Identify the preparation type.
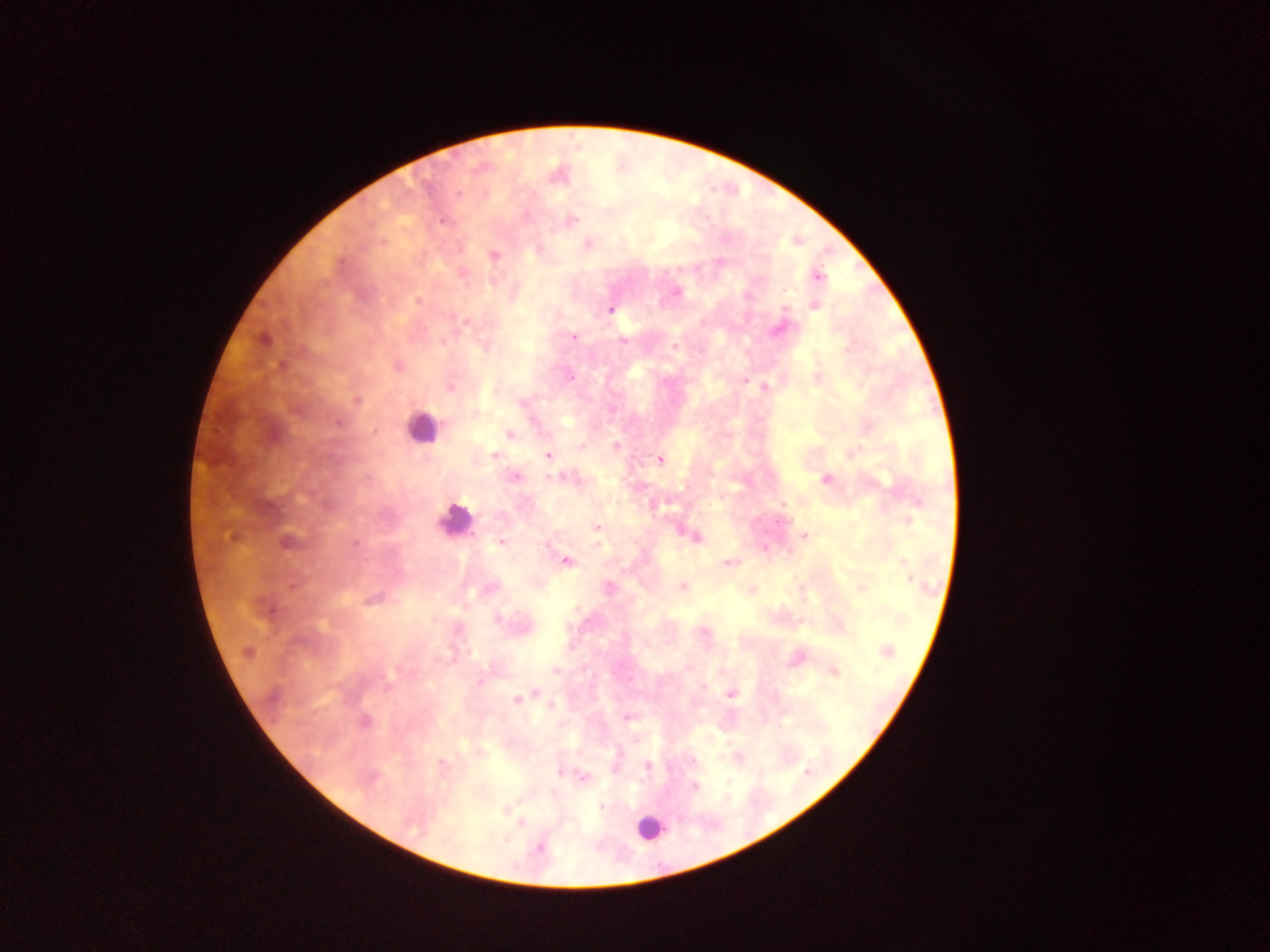

Thick blood film.

Approximate centers as {x, y} in pixels.
Summary:
  - Leukocyte locations: {421, 427}, {456, 526}, {643, 827}
  - Plasmodium parasite locations: {457, 192}, {571, 218}, {588, 244}, {817, 277}, {814, 306}, {609, 309}, {465, 320}, {575, 337}, {620, 339}, {674, 346}, {815, 377}, {744, 380}, {764, 386}, {519, 399}, {510, 433}, {615, 445}, {851, 452}, {548, 455}, {494, 456}, {660, 459}, {514, 476}, {561, 477}, {824, 480}, {909, 519}, {596, 533}, {804, 535}, {501, 542}, {565, 561}, {724, 563}, {902, 564}, {909, 575}, {608, 587}, {681, 587}, {863, 588}, {750, 590}, {704, 631}, {886, 651}, {555, 670}, {834, 673}, {539, 693}, {732, 694}, {515, 698}, {625, 717}, {738, 758}, {647, 766}, {582, 778}, {694, 786}, {600, 806}, {503, 810}, {519, 820}, {539, 847}
  - Image size: 1270×952 pixels
  - Capture: mobile-phone photograph through a microscope
  - Field of view: single
  - Country: Ghana